Outline each blood parasite and name the species.
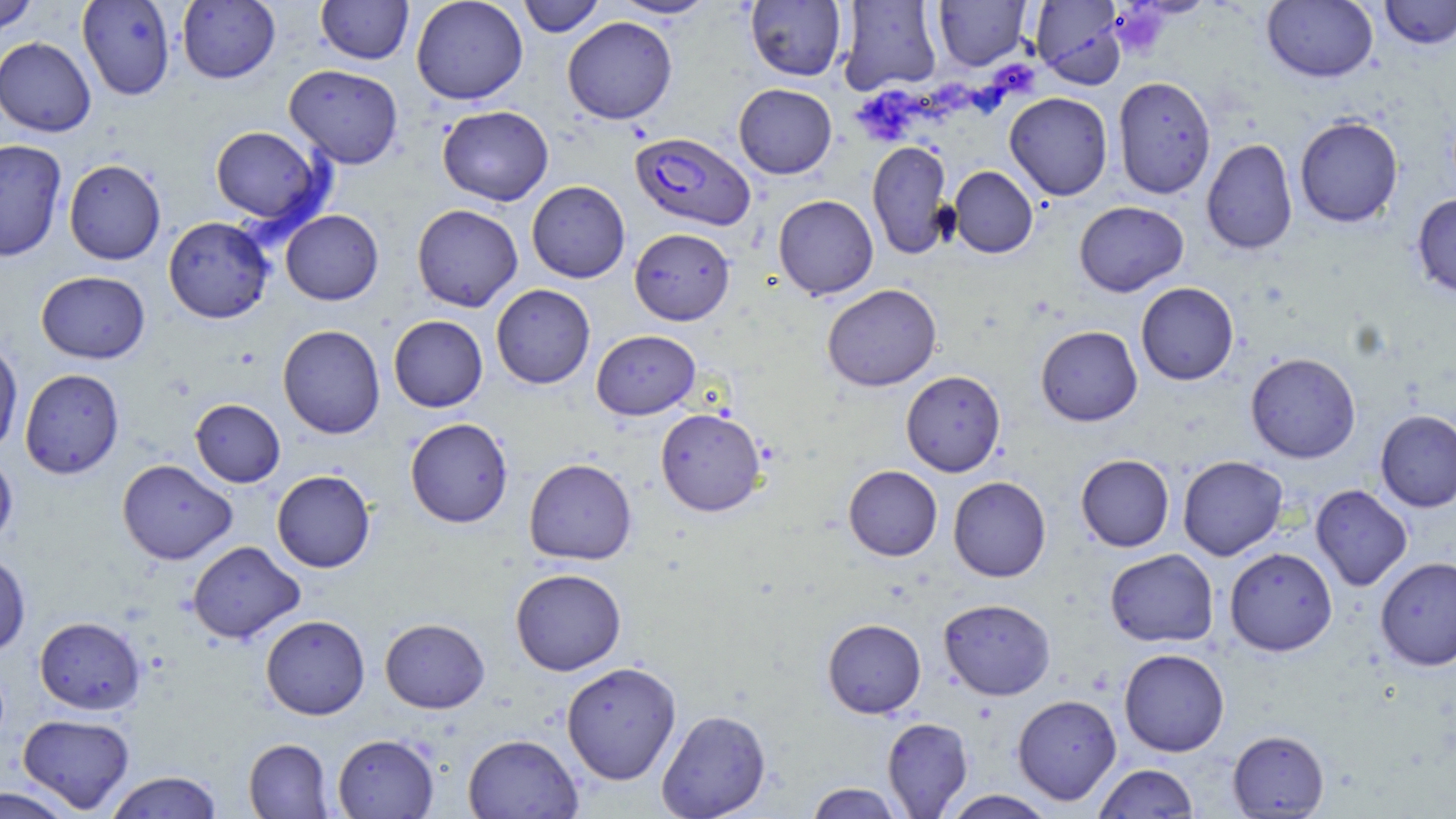

Approximate bounding boxes as (x1, y1, x2, y2) in pixels.
Plasmodium falciparum-infected red blood cells: (629, 131, 755, 231).
No Plasmodium ovale, Plasmodium malariae, Plasmodium vivax, Babesia divergens, or Trypanosoma brucei observed.

Platelet locations: (1109, 5, 1169, 59). Uninfected red blood cell locations: (0, 0, 38, 36), (77, 0, 176, 100), (177, 0, 280, 84), (316, 0, 413, 65), (410, 0, 528, 105), (518, 0, 606, 37), (611, 0, 717, 19), (838, 0, 942, 94), (932, 0, 1030, 70), (1030, 0, 1127, 88), (1379, 0, 1456, 49), (746, 1, 847, 81), (1262, 1, 1378, 82), (562, 16, 677, 124), (0, 36, 95, 137), (284, 64, 403, 168), (1113, 77, 1216, 198), (733, 83, 837, 178), (1005, 92, 1113, 200), (437, 105, 554, 205), (1294, 115, 1403, 227), (209, 125, 327, 226), (1201, 138, 1297, 254), (0, 139, 67, 262), (867, 140, 953, 259), (64, 159, 166, 265), (949, 166, 1038, 258), (526, 181, 630, 283), (1411, 193, 1456, 299), (773, 195, 878, 300), (1074, 201, 1189, 297), (412, 204, 523, 311), (281, 210, 383, 305), (163, 216, 274, 323), (629, 227, 735, 325), (36, 271, 150, 364), (1136, 282, 1239, 385), (491, 284, 595, 389), (822, 284, 942, 391), (388, 315, 487, 412), (277, 324, 385, 438), (1035, 325, 1142, 426), (591, 329, 700, 420), (0, 337, 23, 456), (1245, 352, 1361, 463), (20, 368, 124, 479), (901, 370, 1005, 476), (190, 399, 285, 487), (655, 407, 767, 516), (1375, 409, 1456, 512), (405, 417, 513, 528), (0, 450, 18, 549), (1076, 454, 1174, 552), (1177, 455, 1288, 560), (524, 458, 636, 564), (117, 459, 237, 565), (843, 465, 942, 560), (272, 470, 375, 573), (948, 476, 1051, 582), (1311, 484, 1413, 591), (187, 541, 304, 644), (1224, 547, 1337, 655), (1104, 548, 1219, 647), (0, 552, 31, 656), (1375, 556, 1456, 671), (510, 568, 626, 675), (938, 598, 1056, 700), (260, 615, 370, 720), (34, 616, 145, 714), (380, 618, 490, 713), (822, 618, 926, 718), (1119, 648, 1229, 756), (561, 661, 681, 784), (1012, 694, 1121, 805), (656, 708, 771, 819), (18, 714, 135, 813), (882, 717, 972, 818), (1227, 729, 1329, 817), (333, 734, 439, 818), (463, 734, 583, 818), (244, 738, 334, 818), (1093, 763, 1198, 818), (105, 771, 222, 818), (806, 782, 904, 819), (0, 786, 78, 818), (942, 790, 1057, 818). Slide-level diagnosis: Plasmodium falciparum. Image is 1456×819 pixels. Optical microscopy. 1000x magnification. Thin blood smear. May-Grünwald-Giemsa-stained preparation. Single field of view.